Give the position of every Plasmodium parasite.
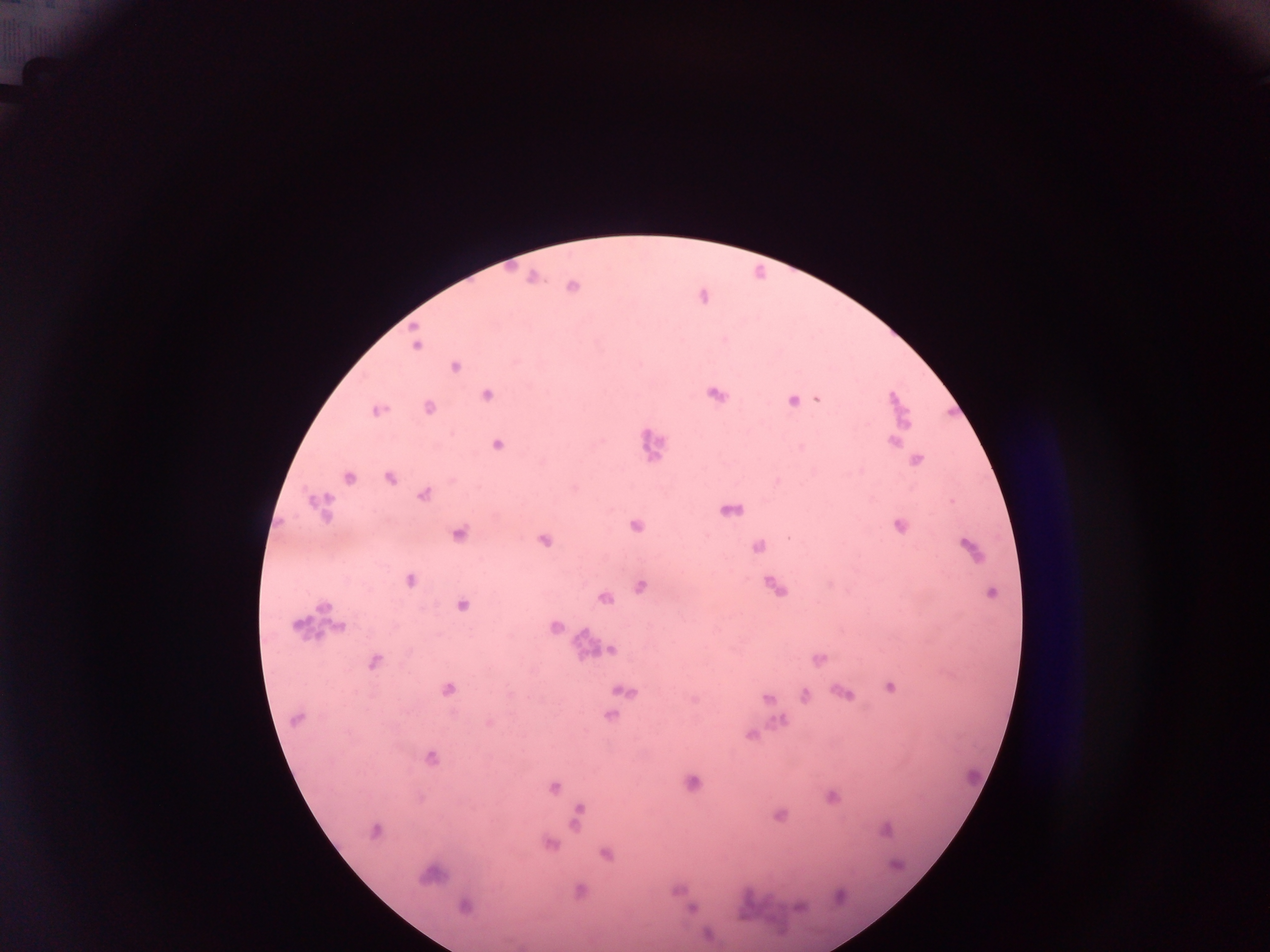
Approximate centers as [x, y] in pixels.
Plasmodium parasites: [532, 278], [571, 286], [414, 344], [455, 366], [714, 393], [486, 394], [792, 399], [817, 399], [428, 407], [376, 410], [891, 440], [497, 444], [915, 460], [348, 477], [389, 477], [423, 494], [319, 504], [728, 509], [635, 525], [900, 525], [457, 533], [543, 539], [758, 547], [970, 548], [409, 579], [773, 585], [639, 586], [990, 591], [603, 597], [461, 605], [340, 627], [553, 627], [610, 649], [818, 659], [373, 661], [889, 686], [447, 689], [621, 691], [842, 692], [803, 694], [767, 698], [609, 715], [297, 718], [489, 723], [750, 735], [429, 757], [692, 783], [553, 786], [831, 797], [578, 814], [778, 815], [376, 830], [885, 830], [549, 843], [605, 853], [430, 874], [580, 890], [464, 905], [693, 908].

Summary:
  - Leukocyte locations: [658, 444], [309, 617], [583, 642]
  - Capture: mobile-phone photograph through a microscope
  - Preparation: thick blood smear
  - Image size: 1270×952 pixels
  - Country: Ghana
  - Field of view: single